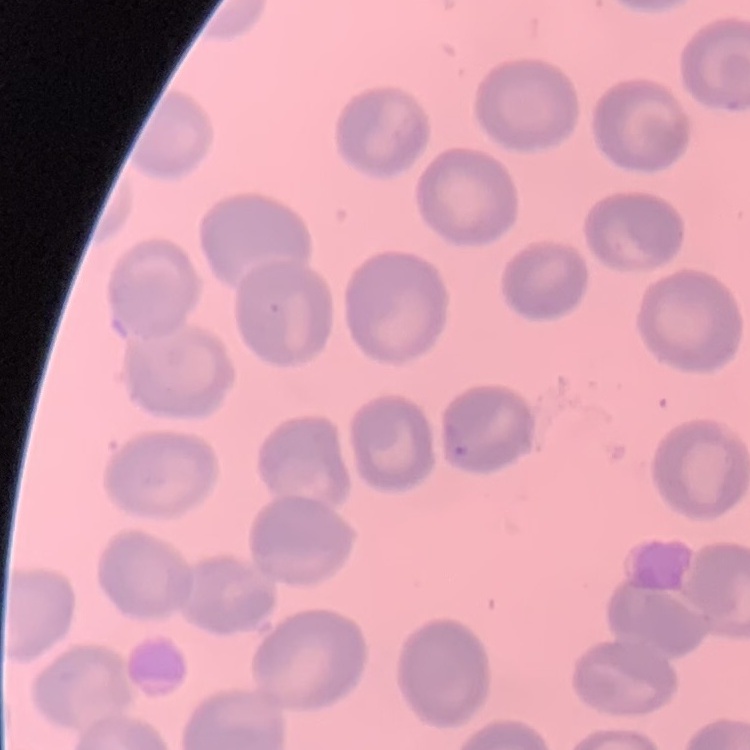

The erythrocytes exhibit no rouleaux formation. One tile cut from a larger photomicrograph. Thin peripheral smear. Field's or Giemsa stain.